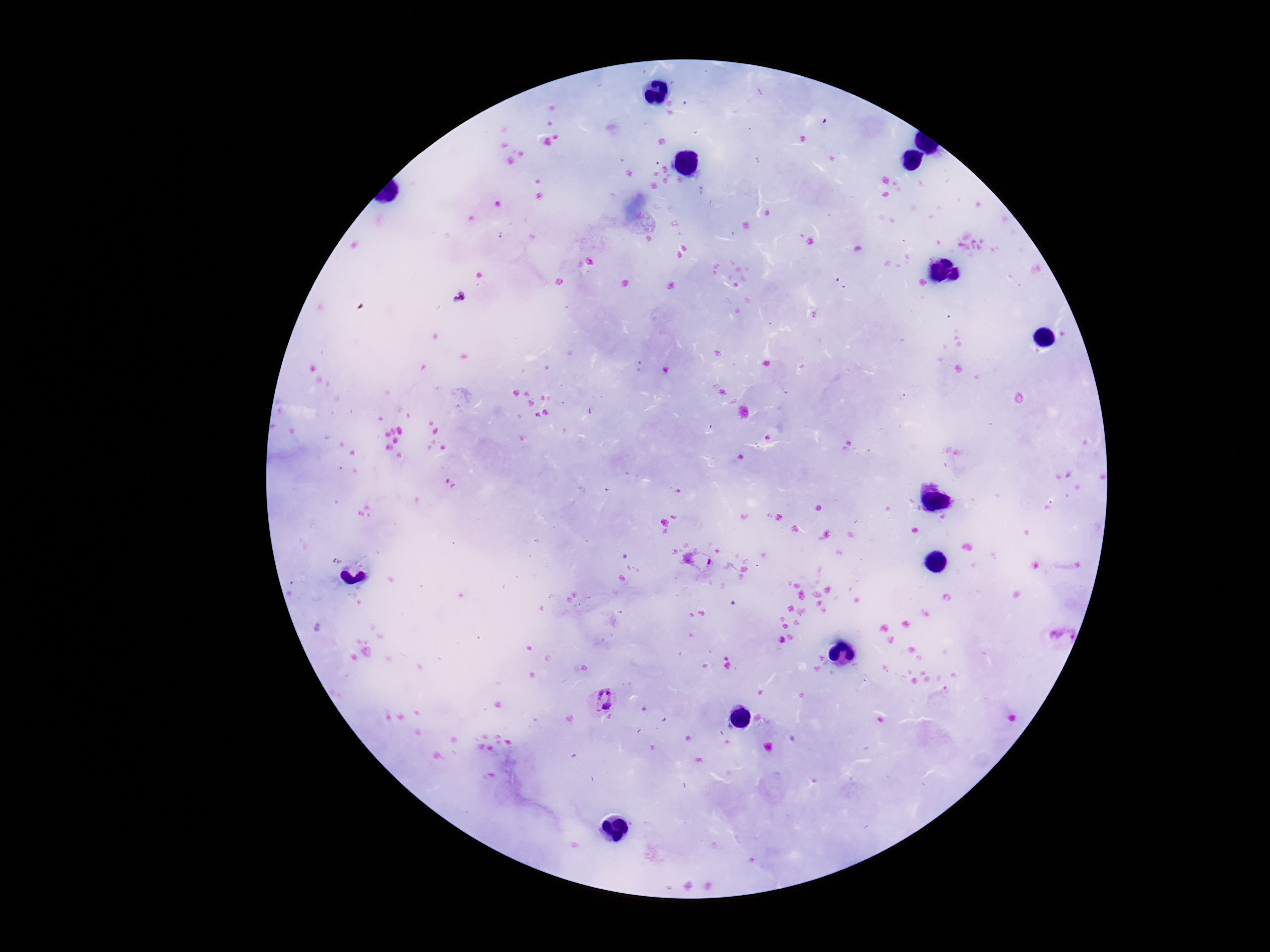

Approximate centers as {x, y} in pixels. Plasmodium parasite locations: {697, 560}, {601, 700}. Smartphone photograph taken through the microscope eyepiece. Thick blood smear. Patient malaria status: positive. Giemsa-stained preparation. Image is 1270×952 pixels. 100x magnification. One field from this slide.